State the preparation type.
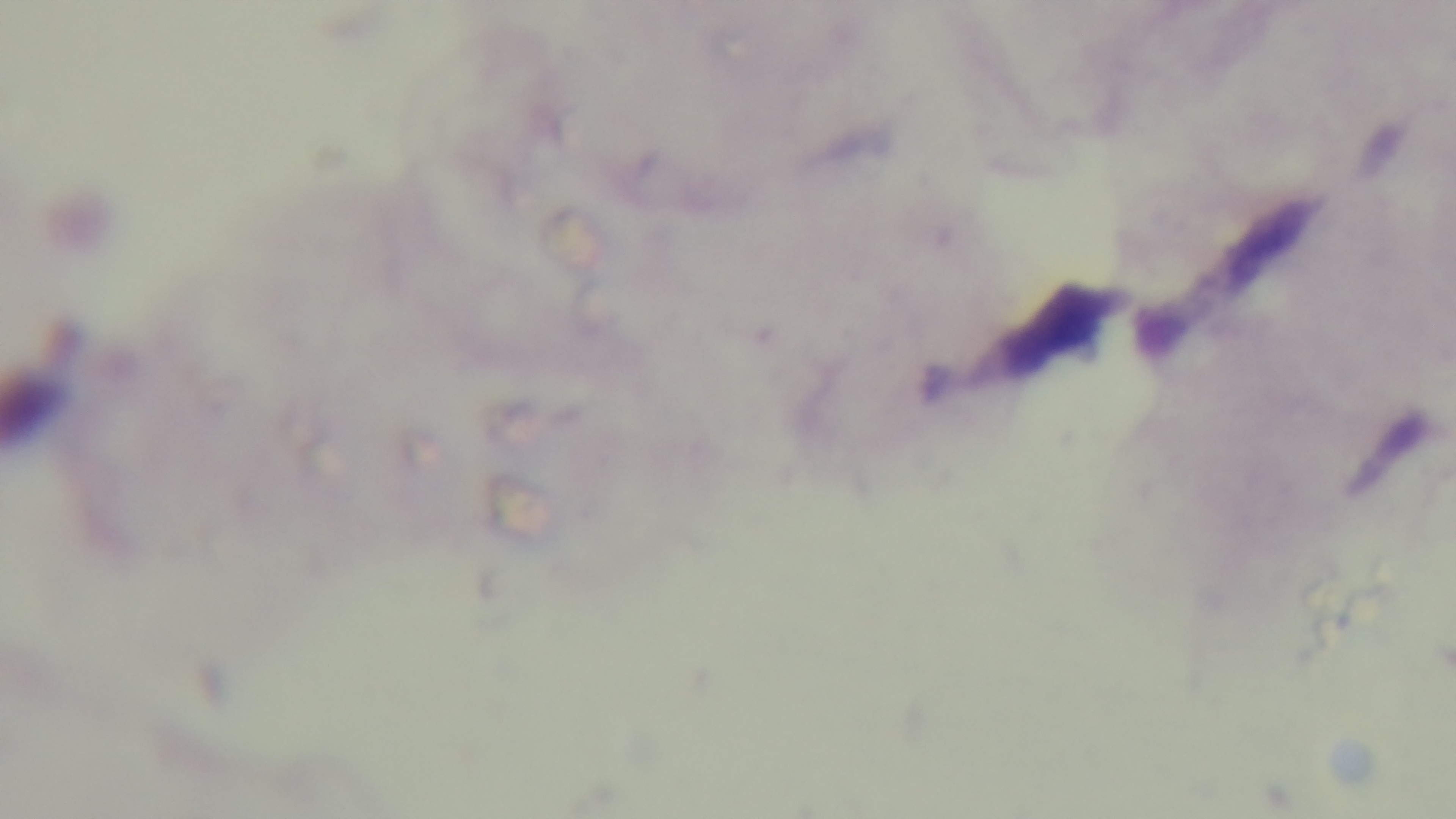

A thick smear.

Summary:
  - Objective: 100x oil immersion
  - Malaria status: uninfected
  - Field of view: single
  - Stain: Giemsa
  - Modality: light microscopy
  - Capture: mounted 4K digital camera